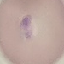
Malaria status: parasitized. Automatically extracted cell patch, resized to 64 × 64 pixels. Giemsa-stained preparation. Thin blood film. Photographed with a smartphone camera at the microscope eyepiece.